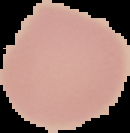
From a thin blood smear. Cell region segmented out of the field of view; the surrounding area is masked to black. Image is 130×133 pixels. Result: no Plasmodium parasites seen.